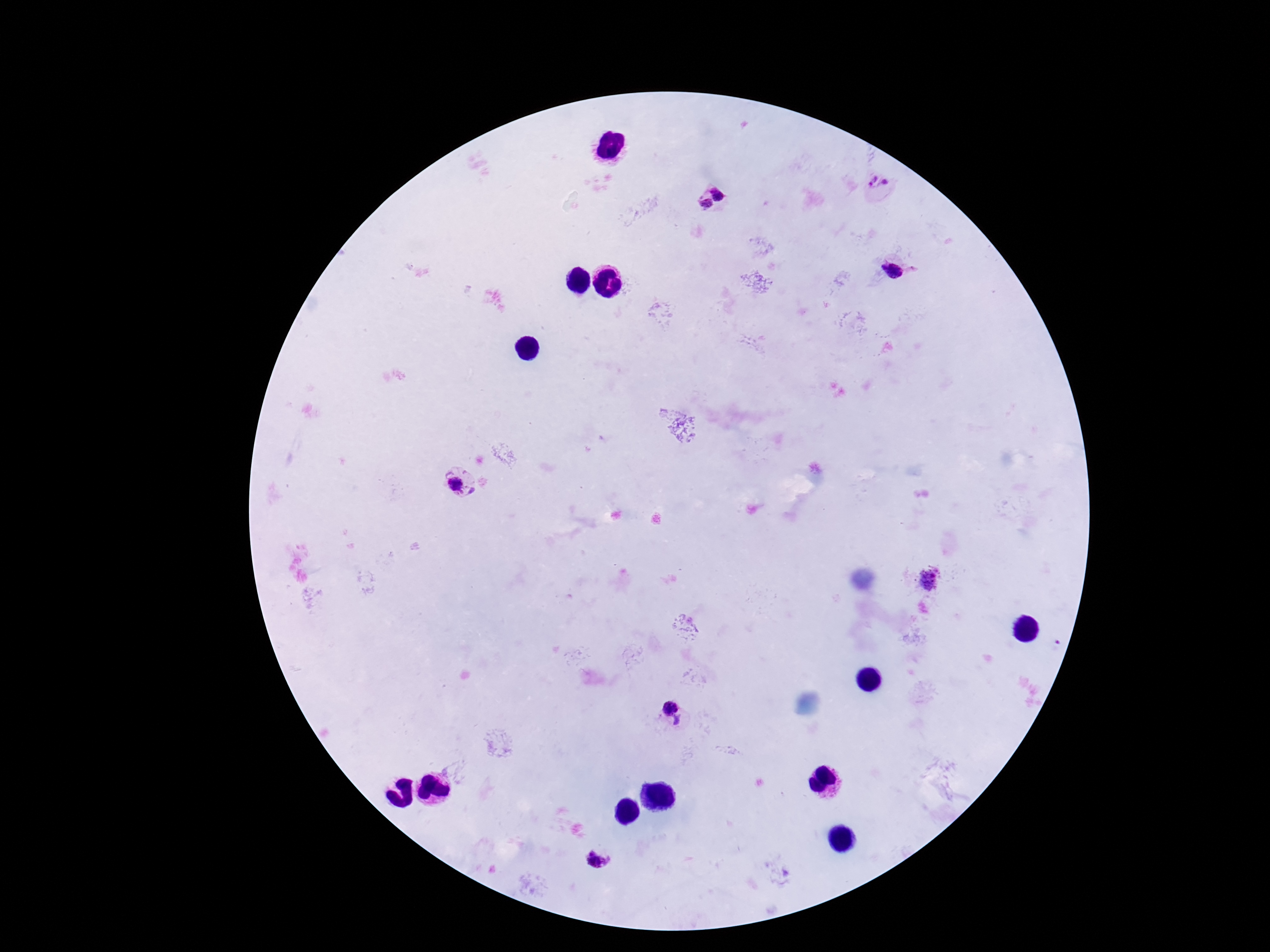

preparation = thick blood film
Plasmodium parasite locations = approximate object centers, in pixels from the top-left corner: (x=879, y=186), (x=722, y=190), (x=705, y=206), (x=893, y=270), (x=458, y=484), (x=929, y=581), (x=669, y=706), (x=678, y=721), (x=599, y=859)
capture = smartphone camera through the microscope eyepiece
patient malaria status = infected
stain = Giemsa
field of view = one from this slide
image size = 1270×952 pixels
magnification = 100x